Assess this cell for malaria.
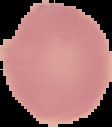

Uninfected.

image type = segmented cell region with the area outside set to black
image size = 112×127 pixels
preparation = thin blood smear